Classify this cell by malaria status.
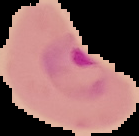

It is parasitized.

image_size: 139×136 pixels
image_type: cell region segmented out of the field of view; surrounding area masked to black
preparation: thin blood smear